Comment on the morphology of the red blood cells.
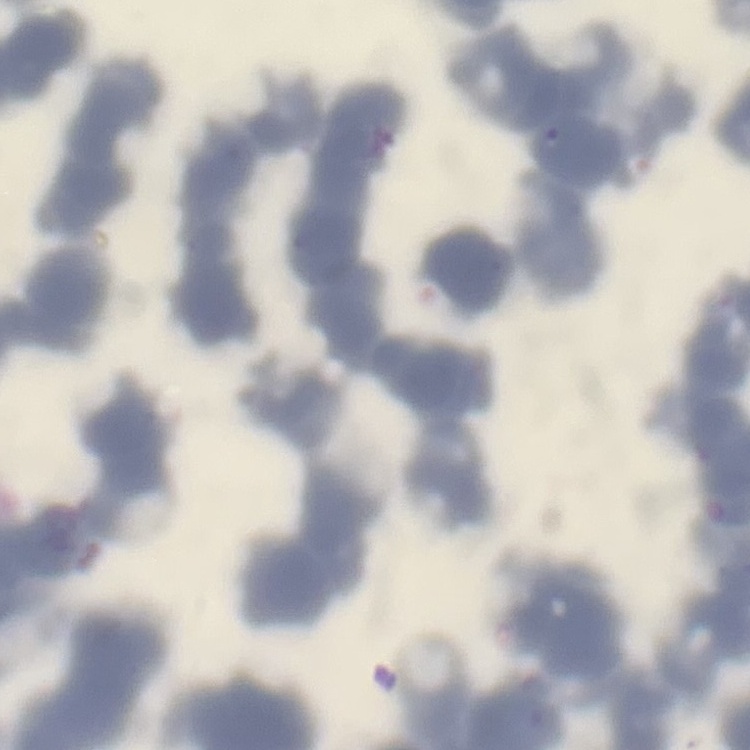

They show rouleaux formation.

stain: Field's or Giemsa
preparation: thin peripheral smear
image_type: one tile cut from a larger photomicrograph